Assess this cell for malaria.
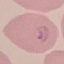

It is parasitized.

Giemsa stain. Thin smear of blood. Photographed with a smartphone camera at the microscope eyepiece. Automatically extracted cell patch, resized to 64 × 64 pixels.